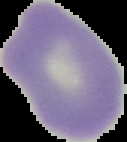 From a thin blood smear. The area outside the segmented cell region is set to black. Image is 127×142 pixels. Result: no malaria parasites detected.